Identify the parasite.
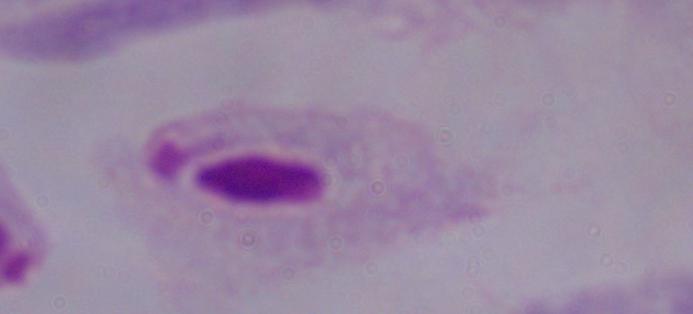
A trichomonad.

magnification = 1000x
modality = micrograph